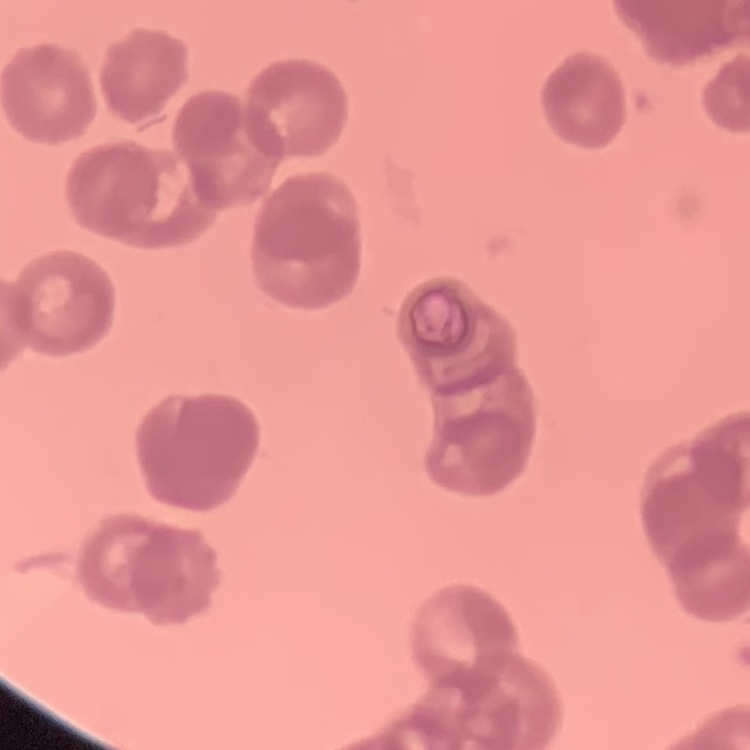

erythrocyte morphology = rouleaux formation
image type = one tile cut from a larger photomicrograph
stain = Field's or Giemsa
preparation = thin blood film